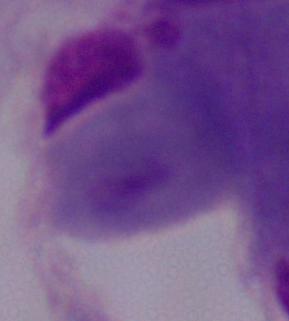 A trichomonad is shown. Micrograph. 1000x magnification.